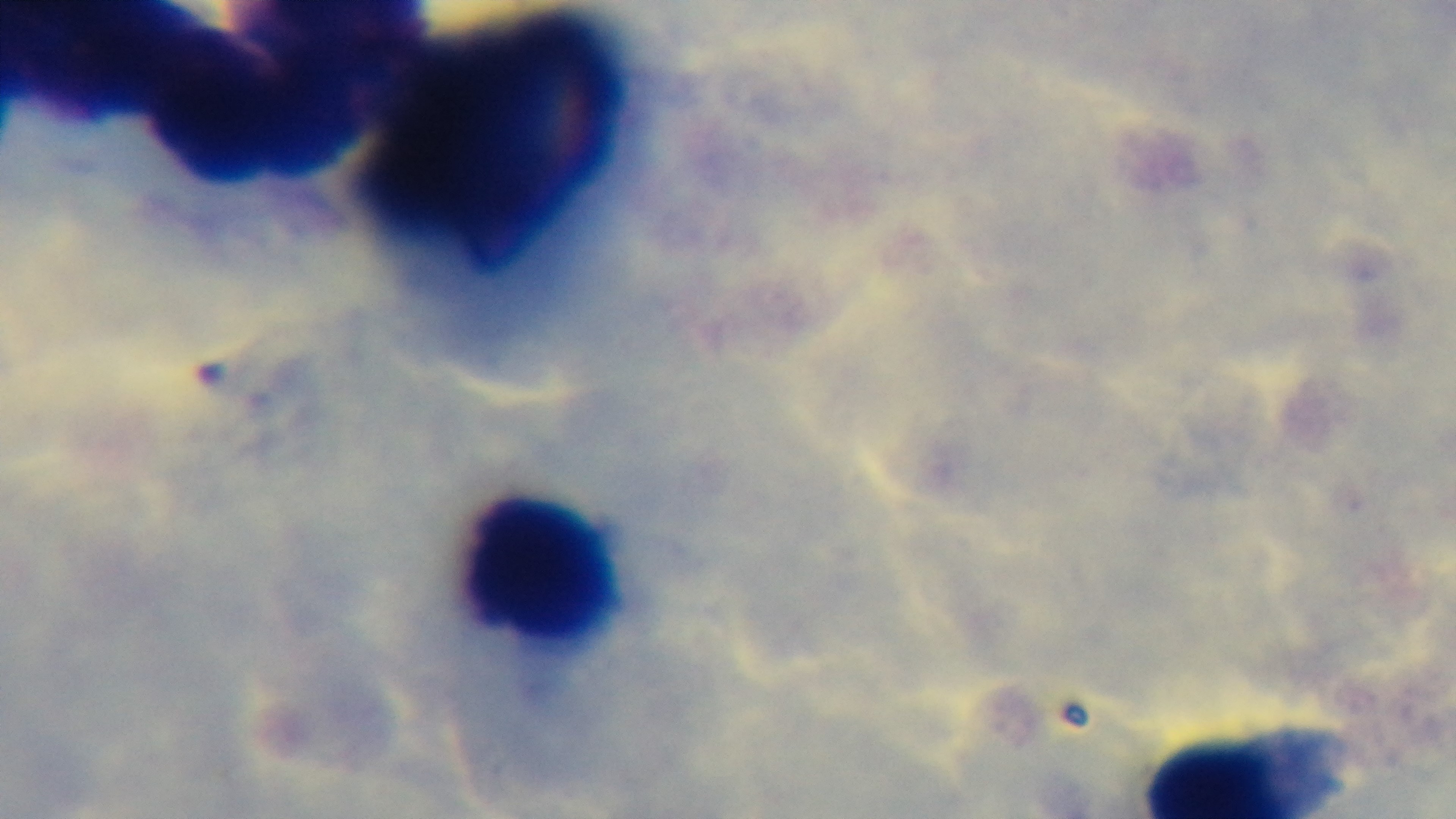
One field from the slide. Preparation: thick blood film. 100x oil-immersion objective. Mounted 4K digital camera. Photomicrograph. Malaria status: negative. Giemsa-stained.